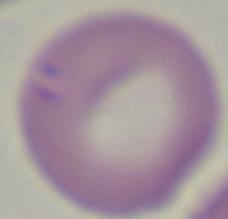 Photomicrograph. Captured at 1000x magnification. A Babesia parasite is shown.